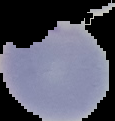 Segmented cell region on a black background. Result: Plasmodium parasites identified. Image is 115×121 pixels. From a thin blood smear.